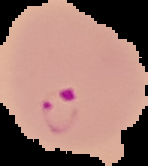

The area outside the segmented cell region is set to black. Result: Plasmodium parasites detected. Image is 148×166 pixels. From a thin blood smear.